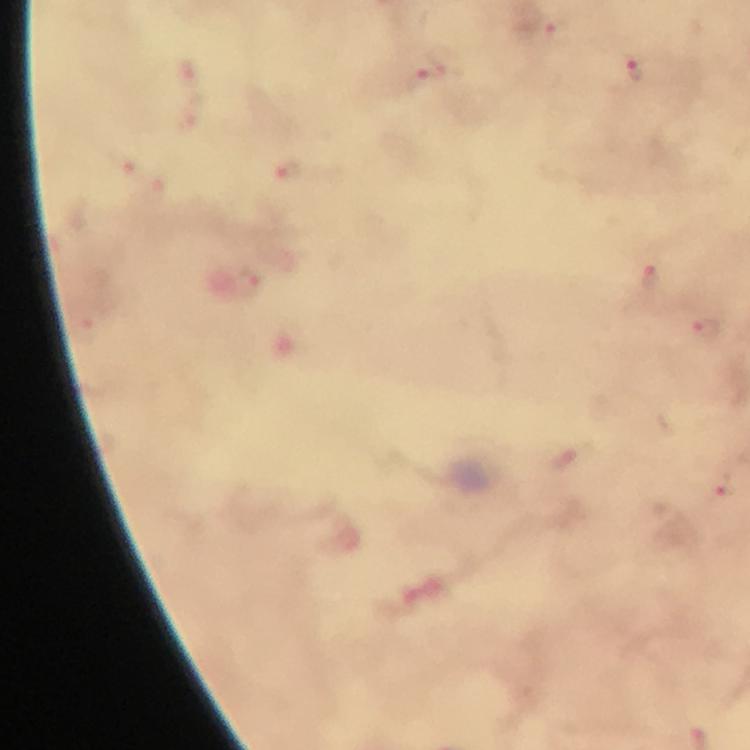

Approximate object centers, in pixels from the top-left corner.
Summary:
  - Malaria parasite locations: (x=558, y=38), (x=436, y=64), (x=635, y=72), (x=649, y=284), (x=706, y=329), (x=724, y=490)
  - Cropped from: one field of view
  - Stain: Giemsa
  - Preparation: thick blood smear
  - Context: from a diagnostic examination for malaria
  - Immersion oil: applied
  - Image size: 750×750 pixels
  - Capture: smartphone mounted on the microscope
  - Magnification: 100x